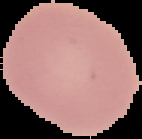
image_type: cell region segmented out of the field of view; surrounding area masked to black
preparation: thin blood film
malaria_status: uninfected
image_size: 142×139 pixels